Outline each blood parasite and name the species.
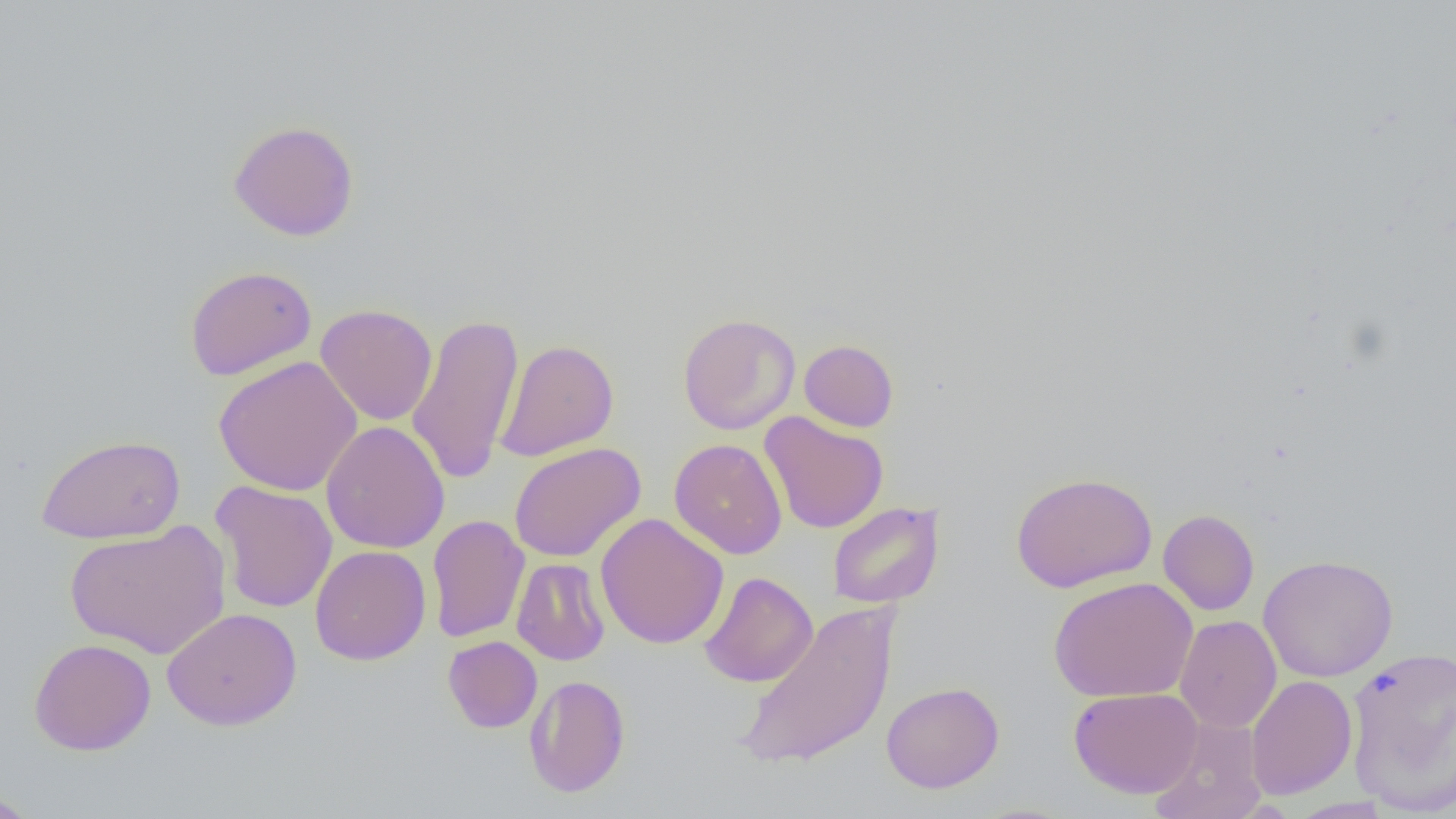

No blood parasites observed.

Approximate bounding boxes as (x1, y1, x2, y2) in pixels. Uninfected red blood cell locations: (228, 119, 360, 241), (185, 265, 317, 381), (315, 304, 438, 426), (406, 311, 524, 486), (677, 313, 800, 435), (496, 339, 619, 461), (799, 339, 899, 432), (214, 355, 362, 496), (759, 412, 889, 533), (321, 420, 450, 553), (35, 433, 186, 544), (670, 438, 787, 559), (509, 442, 646, 563), (1010, 471, 1158, 593), (210, 480, 338, 613), (827, 501, 944, 608), (1158, 509, 1259, 616), (595, 513, 729, 649), (426, 514, 529, 643), (65, 520, 231, 660), (310, 544, 431, 666), (1257, 554, 1398, 682), (512, 558, 611, 665), (699, 571, 818, 687), (1048, 577, 1199, 702), (735, 601, 898, 773), (162, 607, 302, 731), (1175, 615, 1282, 733), (443, 636, 542, 732), (29, 638, 157, 756), (1344, 644, 1456, 814), (524, 674, 631, 798), (1245, 674, 1358, 799), (881, 681, 1004, 793), (1068, 687, 1203, 798), (1153, 716, 1268, 819), (0, 790, 41, 818), (1287, 797, 1393, 818). Slide-level diagnosis: no evidence of blood parasites. Optical microscopy. Thin blood smear. Captured at 1000x magnification. Image is 1456×819 pixels. One field of a larger specimen.